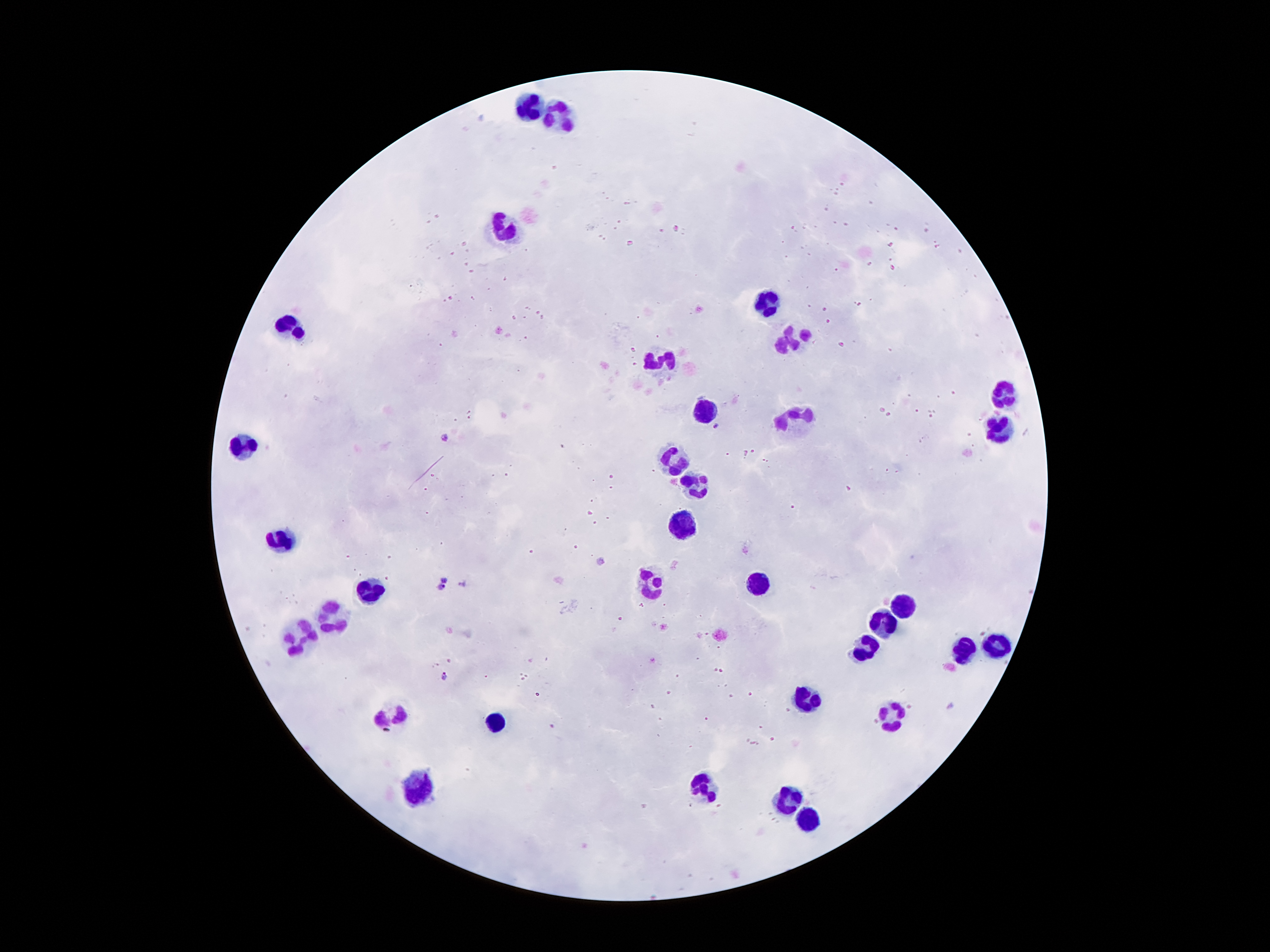

Approximate centers as [x, y] in pixels.
Summary:
  - Leukocyte locations: [530, 101], [565, 113], [504, 232], [768, 301], [287, 321], [794, 339], [661, 359], [1005, 394], [707, 408], [788, 426], [1000, 431], [243, 449], [675, 458], [687, 484], [684, 521], [278, 539], [652, 585], [759, 585], [368, 591], [904, 605], [330, 614], [887, 620], [298, 634], [863, 643], [991, 649], [959, 652], [803, 695], [892, 709], [391, 712], [498, 718], [423, 785], [701, 791], [788, 799], [805, 822]
  - Malaria parasite locations: [716, 427], [444, 437], [601, 561], [445, 579], [462, 582], [441, 589], [445, 676], [950, 707]
  - Stain: Giemsa
  - Field of view: single
  - Magnification: 100x
  - Capture: smartphone camera through the microscope eyepiece
  - Preparation: thick peripheral-blood smear
  - Image size: 1270×952 pixels
  - Patient malaria status: infected with Plasmodium falciparum